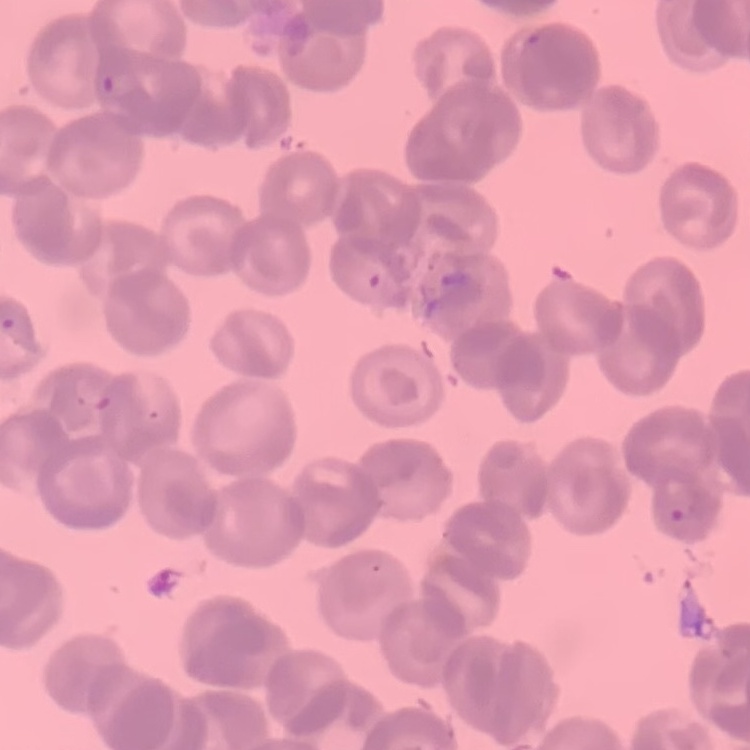
The red blood cells exhibit rouleaux formation. Thin blood smear. Stained with either Field's or Giemsa. Square crop of a larger photomicrograph.